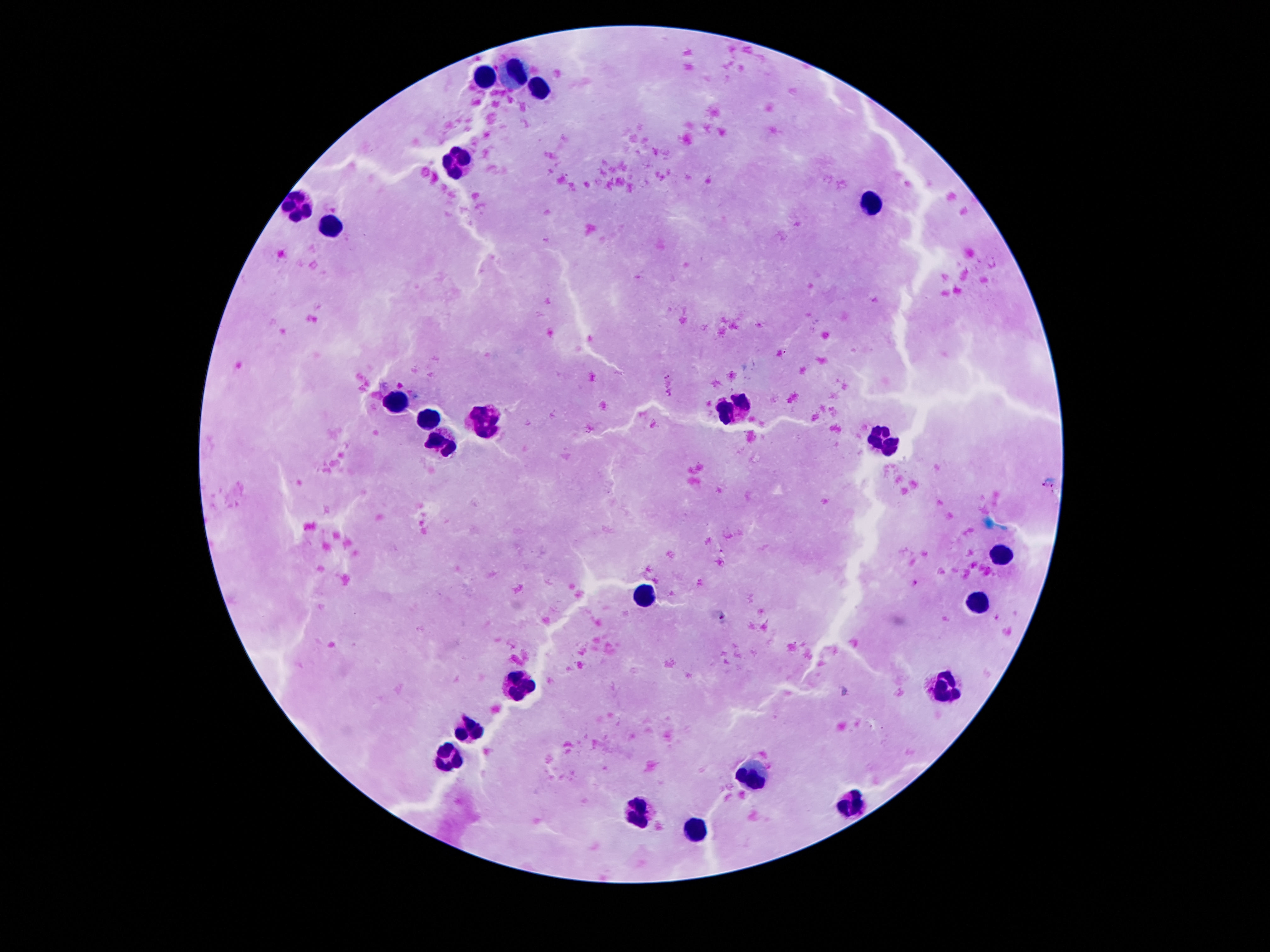

Approximate centers as [x, y] in pixels. Leukocyte locations: [479, 73], [515, 74], [537, 87], [457, 162], [873, 200], [302, 204], [338, 228], [397, 401], [734, 411], [428, 423], [486, 425], [882, 436], [439, 447], [1001, 555], [645, 594], [979, 598], [519, 682], [942, 691], [468, 730], [444, 758], [751, 773], [853, 806], [636, 814], [698, 828]. 100x magnification. Giemsa stain. Image is 1270×952 pixels. Patient malaria status: uninfected. Thick peripheral-blood smear. One field from this slide. Smartphone photograph taken through the microscope eyepiece.